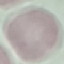

Result: no malaria parasites seen. Cell patch, automatically extracted from a larger field of view and resized to 64 × 64 pixels. Thin blood smear. Giemsa stain. Acquired by smartphone through the microscope eyepiece.